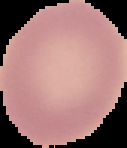
Image is 127×148 pixels. The area outside the segmented cell region is set to black. Malaria status: uninfected. From a thin blood smear.